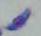

Toxoplasma gondii is seen. Captured at 1000x magnification. Photomicrograph.